Identify the parasite.
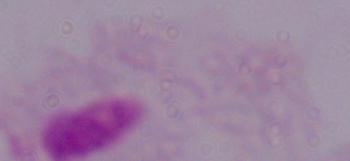

A trichomonad.

Photomicrograph. 1000x magnification.